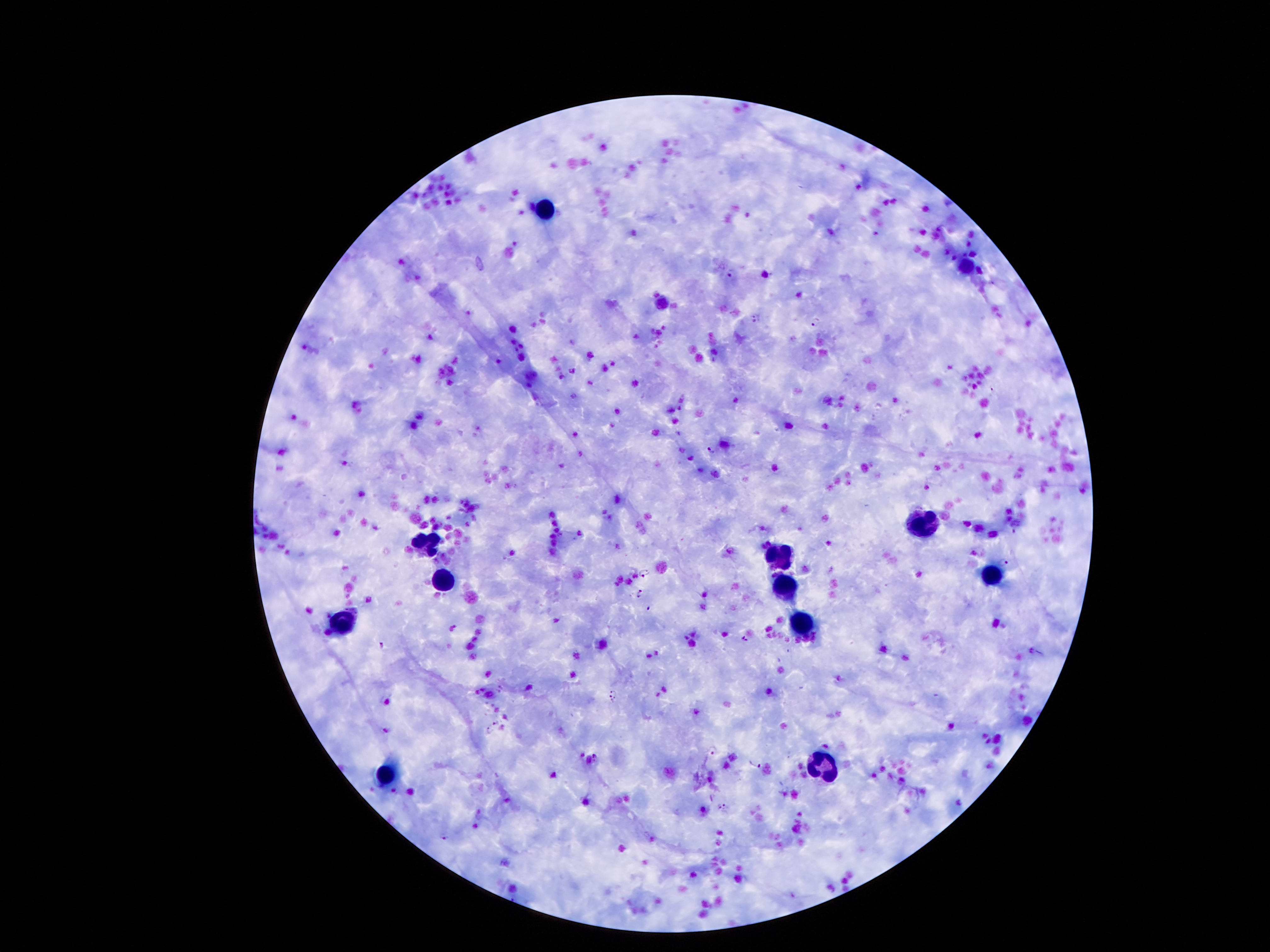

Approximate centers as {x, y} in pixels.
Summary:
  - Leukocyte locations: {542, 210}, {928, 521}, {424, 544}, {778, 553}, {442, 578}, {992, 580}, {787, 587}, {342, 623}, {799, 630}, {821, 764}, {385, 780}
  - Plasmodium parasite locations: {875, 234}, {732, 272}, {756, 318}, {815, 322}, {710, 451}, {1003, 562}, {646, 571}, {639, 593}, {649, 609}, {745, 640}, {381, 644}, {614, 691}, {612, 699}, {496, 722}, {489, 729}, {713, 749}, {595, 755}, {756, 765}, {726, 806}, {718, 807}, {443, 837}
  - Field of view: single
  - Magnification: 100x
  - Preparation: thick blood film
  - Image size: 1270×952 pixels
  - Patient malaria status: positive for Plasmodium falciparum
  - Capture: smartphone camera through the microscope eyepiece
  - Stain: Giemsa